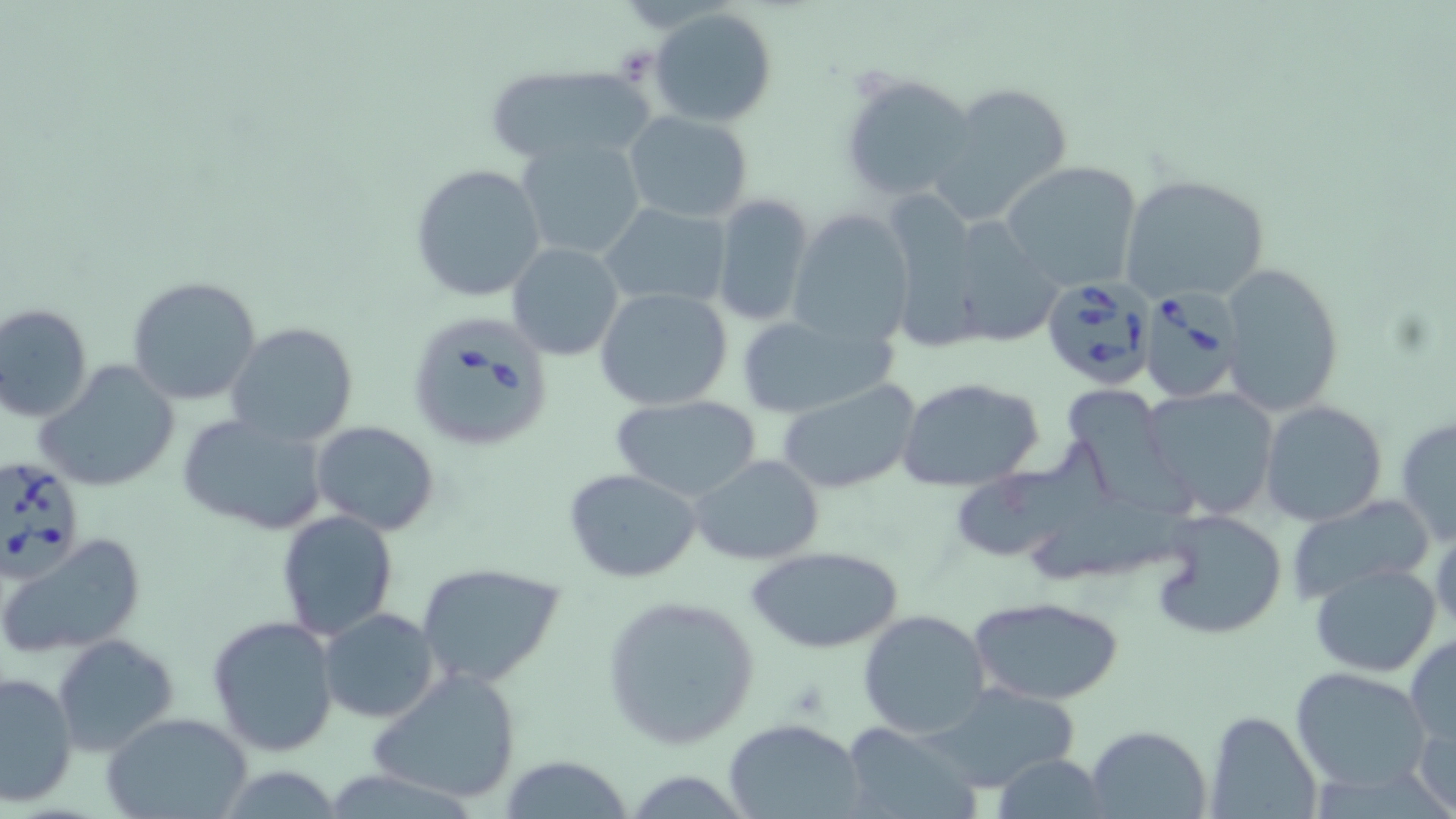
slide-level diagnosis = Babesia divergens
uninfected red blood cell locations = approximate bounding boxes as (x1, y1, x2, y2) in pixels: (650, 8, 777, 126), (483, 65, 656, 168), (840, 69, 979, 206), (930, 82, 1074, 227), (622, 111, 755, 225), (515, 136, 649, 262), (999, 160, 1143, 293), (409, 162, 547, 304), (1117, 174, 1271, 304), (708, 193, 819, 328), (897, 195, 990, 357), (598, 202, 734, 309), (962, 206, 1065, 341), (786, 213, 914, 348), (506, 241, 624, 361), (1218, 262, 1345, 417), (127, 275, 262, 406), (594, 286, 734, 410), (0, 302, 94, 422), (733, 312, 905, 420), (226, 322, 360, 450), (35, 361, 182, 493), (897, 378, 1045, 490), (776, 379, 922, 496), (1139, 386, 1280, 518), (1067, 394, 1202, 535), (611, 395, 761, 501), (1259, 399, 1388, 526), (176, 412, 331, 537), (1394, 414, 1456, 547), (310, 420, 441, 534), (955, 434, 1108, 567), (689, 455, 825, 565), (564, 468, 703, 584), (1034, 495, 1198, 581), (1288, 496, 1438, 602), (1150, 508, 1288, 640), (276, 511, 400, 643), (1, 533, 146, 657), (745, 544, 905, 654), (415, 562, 565, 688), (1309, 563, 1442, 677), (599, 594, 761, 752), (970, 595, 1124, 707), (317, 607, 441, 723), (857, 609, 991, 740), (207, 615, 340, 756), (51, 633, 180, 755), (1405, 634, 1456, 750), (367, 666, 525, 807), (1291, 666, 1430, 790), (0, 671, 78, 807), (926, 682, 1086, 793), (1413, 708, 1456, 818), (1203, 709, 1324, 819), (102, 712, 252, 819), (723, 719, 864, 819), (841, 723, 978, 818), (1085, 725, 1213, 819), (498, 756, 632, 818), (990, 756, 1115, 817)
stain = May-Grünwald-Giemsa
modality = light microscopy
magnification = 1000x
image size = 1456×819 pixels
preparation = thin blood film
field of view = one of a larger specimen
Babesia divergens-infected red blood cell locations = approximate bounding boxes as (x1, y1, x2, y2) in pixels: (1039, 277, 1157, 393), (1137, 287, 1242, 405), (404, 312, 551, 452), (0, 456, 87, 580)